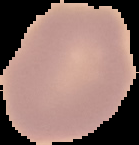

Segmented cell region on a black background. From a thin blood smear. Malaria status: uninfected. Image is 139×145 pixels.